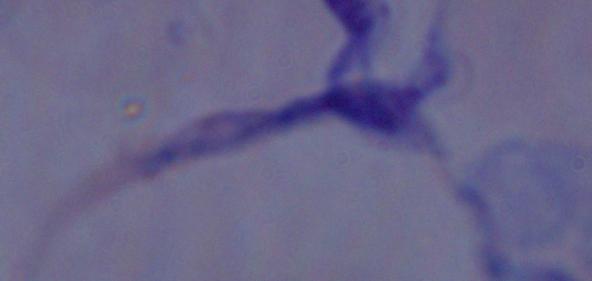

{
  "magnification": "1000x",
  "modality": "photomicrograph",
  "identification": "trypanosome"
}